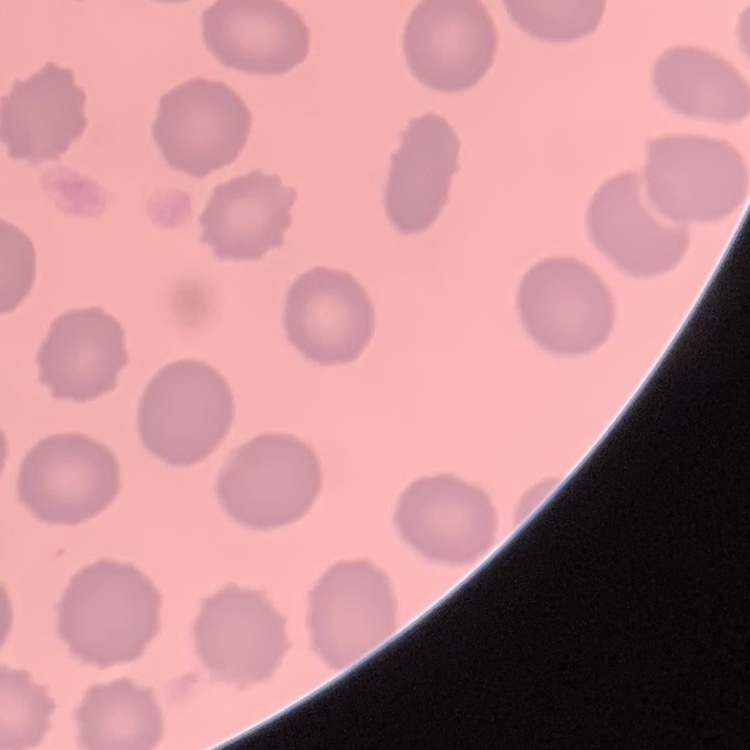

Summary:
  - Red blood cell morphology: no rouleaux formation
  - Image type: one tile cut from a larger photomicrograph
  - Stain: Field's or Giemsa
  - Preparation: thin peripheral smear